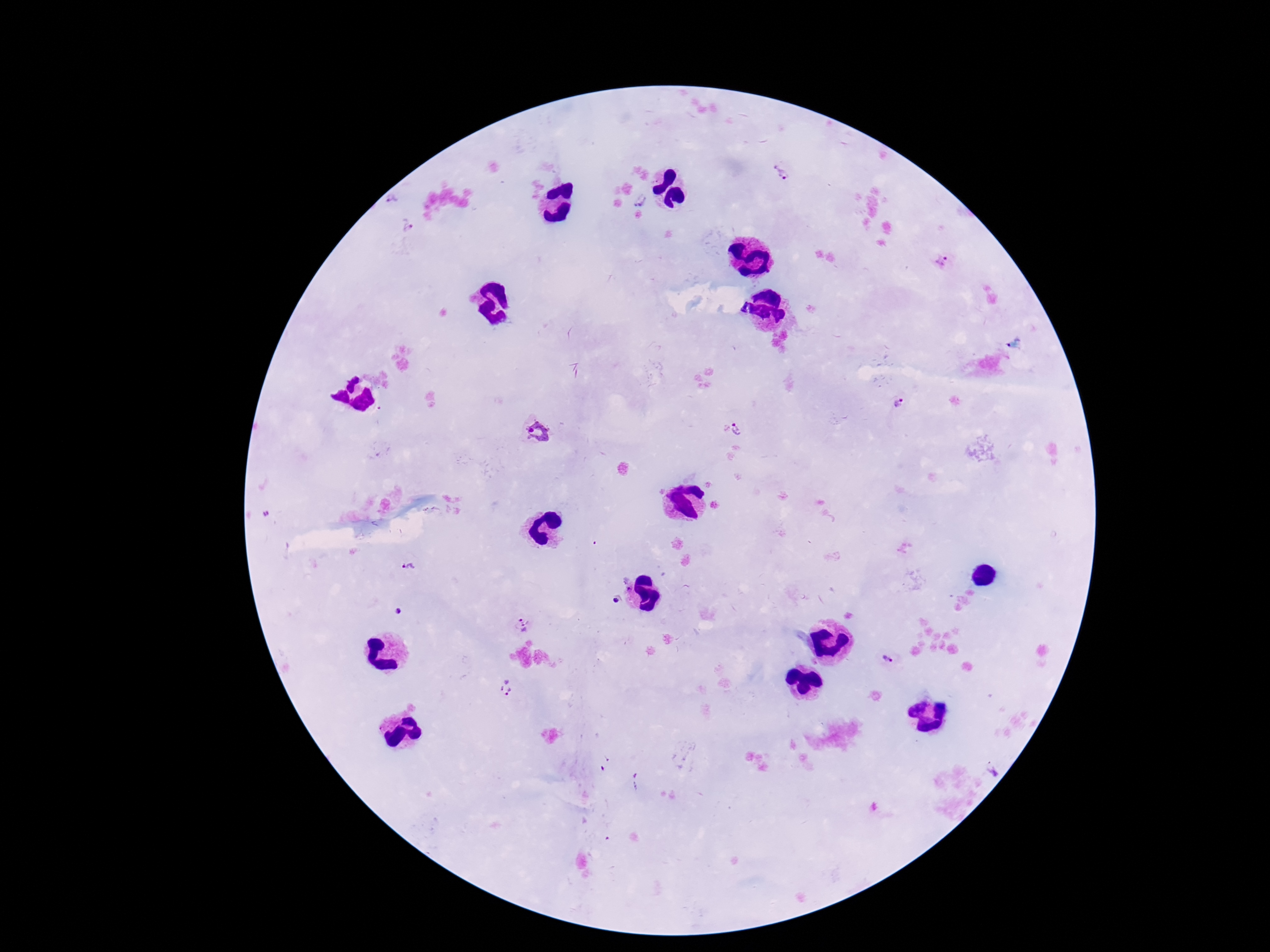
Approximate centers as (x, y) in pixels.
Summary:
  - Plasmodium parasite locations: (783, 173), (394, 198), (641, 202), (407, 226), (943, 260), (897, 402), (740, 429), (538, 433), (409, 567), (616, 601), (397, 612), (522, 625), (886, 660), (506, 689), (992, 767)
  - Patient malaria status: positive
  - Preparation: thick blood film
  - Image size: 1270×952 pixels
  - Magnification: 100x
  - Capture: smartphone camera through the microscope eyepiece
  - Field of view: one from this slide
  - Stain: Giemsa